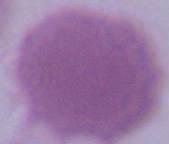
Captured at 1000x magnification. A red blood cell is seen. Photomicrograph.